Assess this cell for malaria.
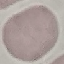
It is uninfected.

{
  "capture": "smartphone camera at the microscope eyepiece",
  "image_type": "cell patch, automatically extracted from a larger field of view and resized to 64 × 64 pixels",
  "stain": "Giemsa",
  "preparation": "thin blood smear"
}